Classify this cell by malaria status.
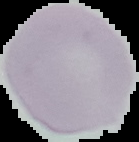
It is uninfected.

image type = cell region segmented out of the field of view; surrounding area masked to black
preparation = thin blood film
image size = 139×142 pixels